Classify this cell by malaria status.
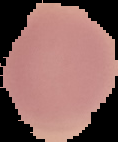

It is uninfected.

Summary:
  - Image size: 118×142 pixels
  - Preparation: thin blood film
  - Image type: segmented cell region on a black background